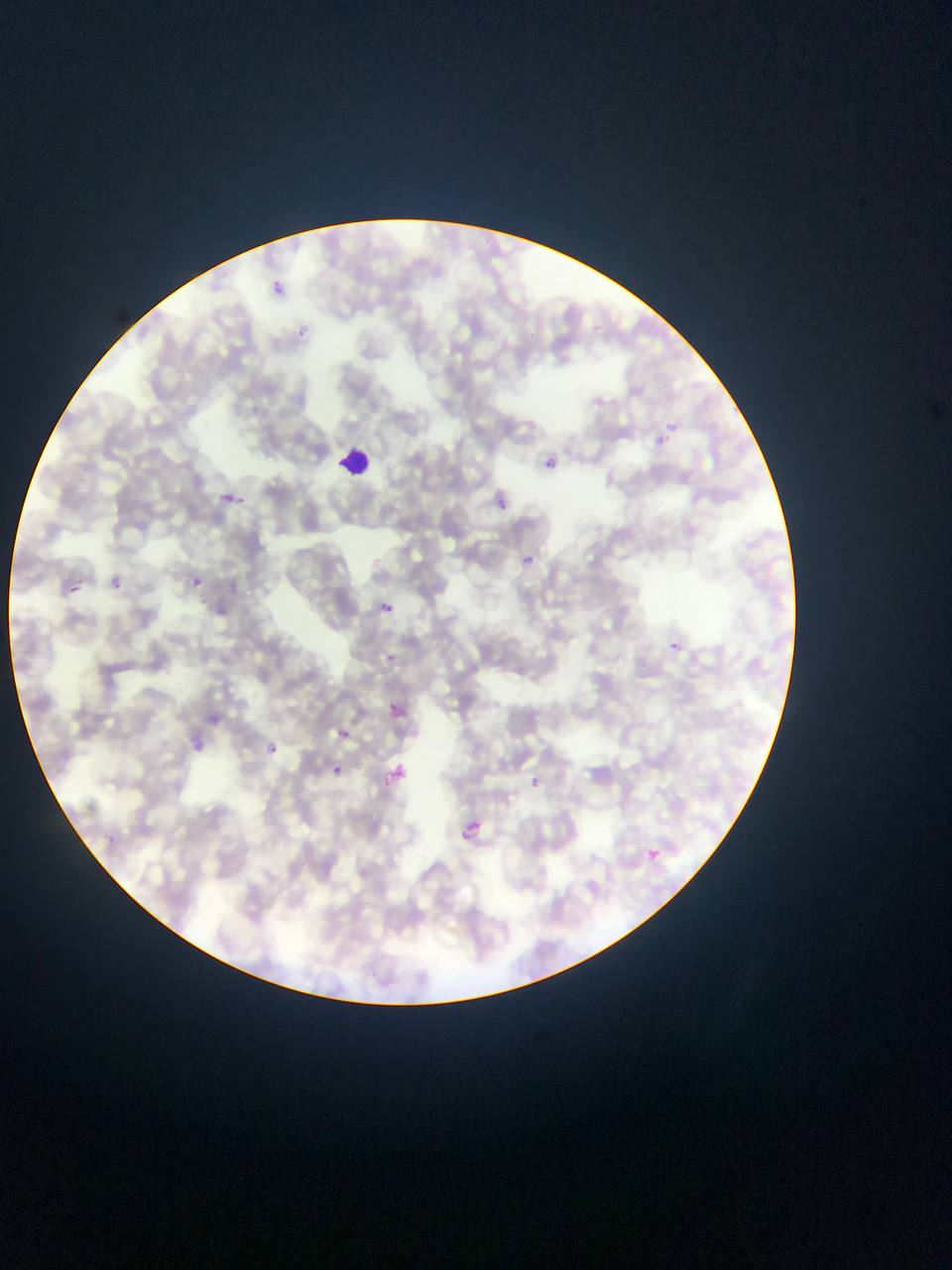

Approximate bounding boxes as [left, top, right, bottom] in pixels. Plasmodium parasite locations: [274, 274, 283, 298], [294, 323, 310, 339], [658, 432, 671, 449], [545, 457, 561, 466], [217, 487, 250, 513], [497, 499, 508, 510], [516, 548, 540, 568], [192, 576, 202, 586], [113, 579, 122, 588], [72, 585, 80, 593], [376, 601, 406, 626], [666, 637, 684, 651], [383, 697, 407, 721], [200, 706, 234, 726], [342, 730, 350, 738], [191, 734, 206, 753], [269, 743, 277, 751], [327, 762, 347, 780], [387, 766, 409, 779], [527, 775, 562, 792], [461, 821, 483, 841], [647, 849, 660, 860]. Leukocyte locations: [336, 443, 375, 479]. Photographed through a microscope with a mobile-phone camera. Thin blood film. Sample from Ghana. Single field of view. Image is 952×1270 pixels.